Locate every leukocyte (white blood cell).
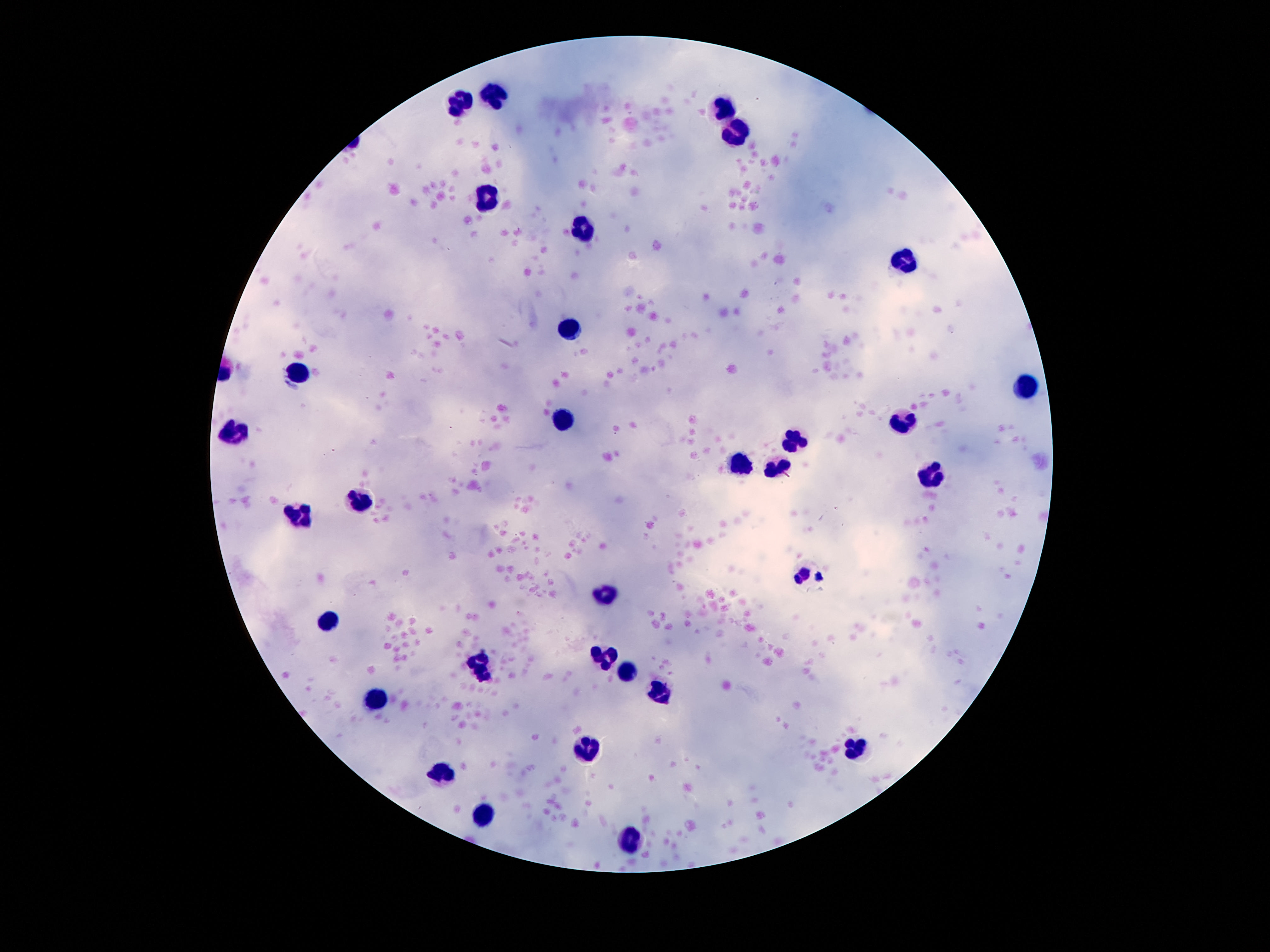
Approximate centers as (x, y) in pixels.
Leukocytes: (498, 96), (460, 103), (721, 111), (736, 138), (489, 202), (582, 231), (904, 260), (570, 330), (301, 369), (1027, 388), (565, 418), (901, 420), (236, 433), (792, 439), (738, 464), (777, 465), (929, 476), (358, 501), (299, 516), (808, 574), (607, 590), (330, 619), (603, 659), (482, 667), (631, 674), (661, 691), (377, 698), (589, 745), (857, 745), (444, 773), (486, 813), (633, 843).

{
  "field_of_view": "one from this slide",
  "magnification": "100x",
  "capture": "smartphone camera through the microscope eyepiece",
  "patient_malaria_status": "negative",
  "image_size": "1270×952 pixels",
  "preparation": "thick peripheral-blood smear",
  "stain": "Giemsa"
}